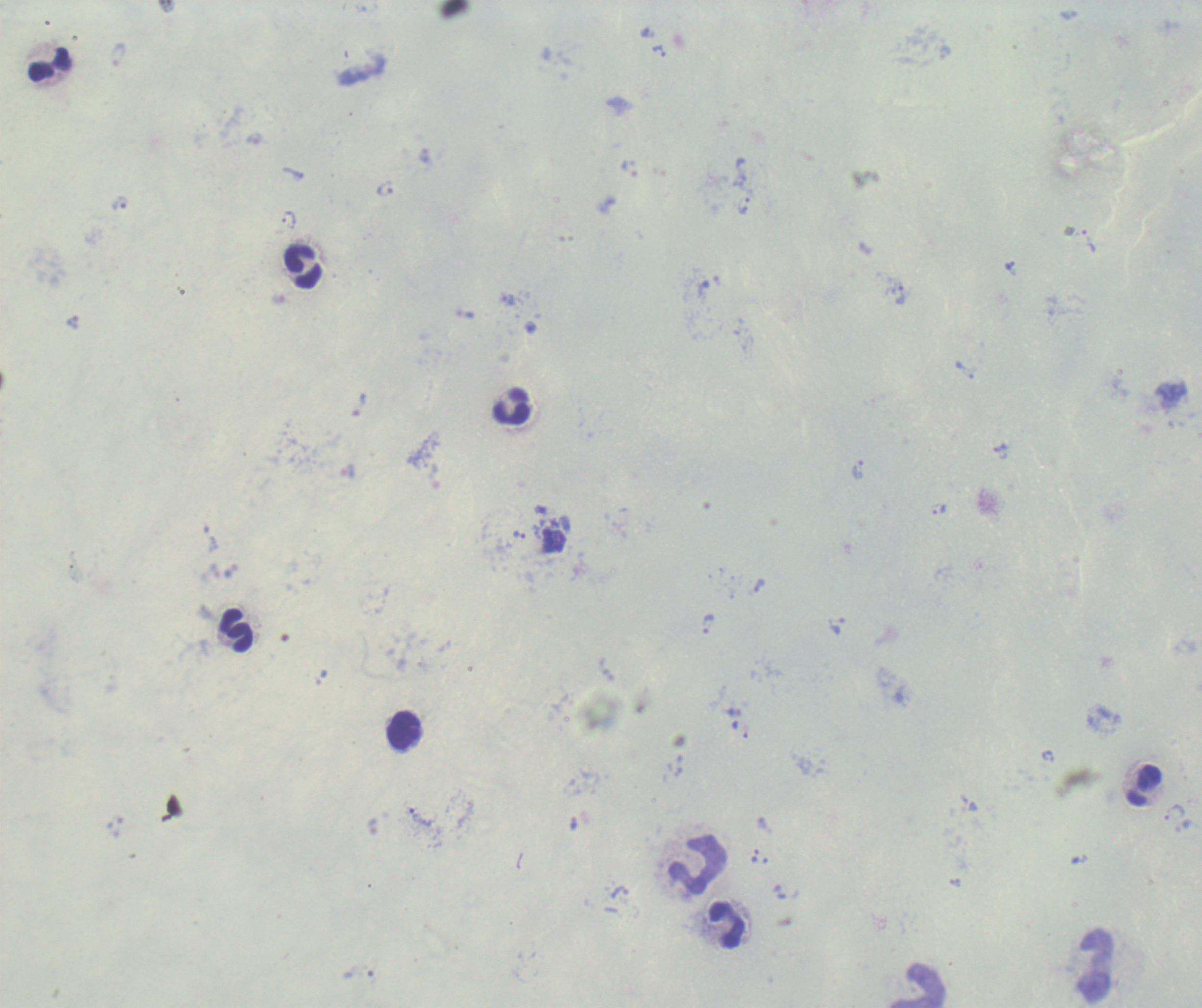
Approximate object centers, in pixels from the top-left corner.
Summary:
  - Leukocyte locations: (x=49, y=63), (x=303, y=267), (x=511, y=408), (x=237, y=630), (x=403, y=730), (x=1144, y=786), (x=697, y=863), (x=726, y=925), (x=1096, y=965), (x=918, y=986)
  - Trophozoite locations: (x=659, y=51), (x=385, y=188), (x=120, y=203), (x=743, y=204), (x=289, y=220), (x=1009, y=266), (x=900, y=295), (x=507, y=300), (x=465, y=314), (x=358, y=404), (x=1001, y=452), (x=857, y=470), (x=937, y=509), (x=519, y=534), (x=759, y=586), (x=708, y=624), (x=837, y=626), (x=1048, y=757), (x=1174, y=812), (x=420, y=817)
  - Stain: Romanowsky
  - Preparation: thick smear of blood
  - Result: positive for malaria parasites
  - Field of view: single
  - Magnification: 100x
  - Context: previously used in a real diagnosis
  - Image size: 1202×1008 pixels
  - Background quality: poor